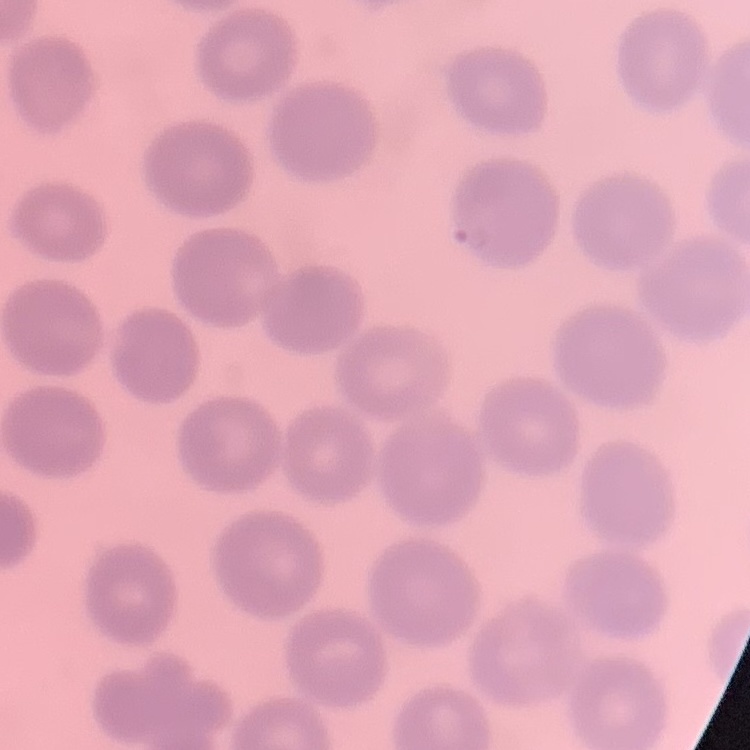
red blood cell morphology = no rouleaux formation
image type = square crop of a larger photomicrograph
preparation = thin peripheral smear
stain = Field's or Giemsa